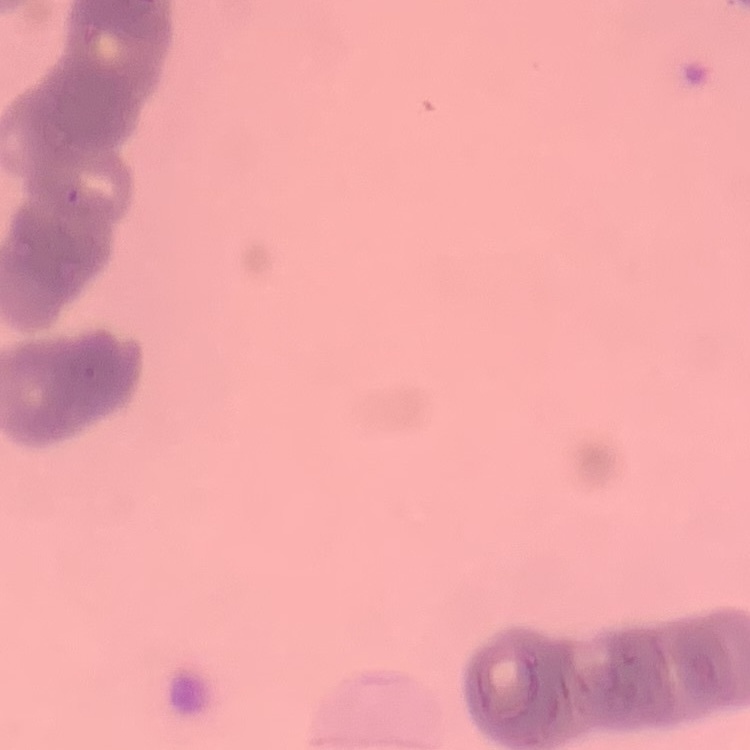
Summary:
  - Red blood cell morphology: rouleaux formation
  - Image type: square crop of a larger photomicrograph
  - Stain: Field's or Giemsa
  - Preparation: thin blood film